Assess the morphology of the erythrocytes.
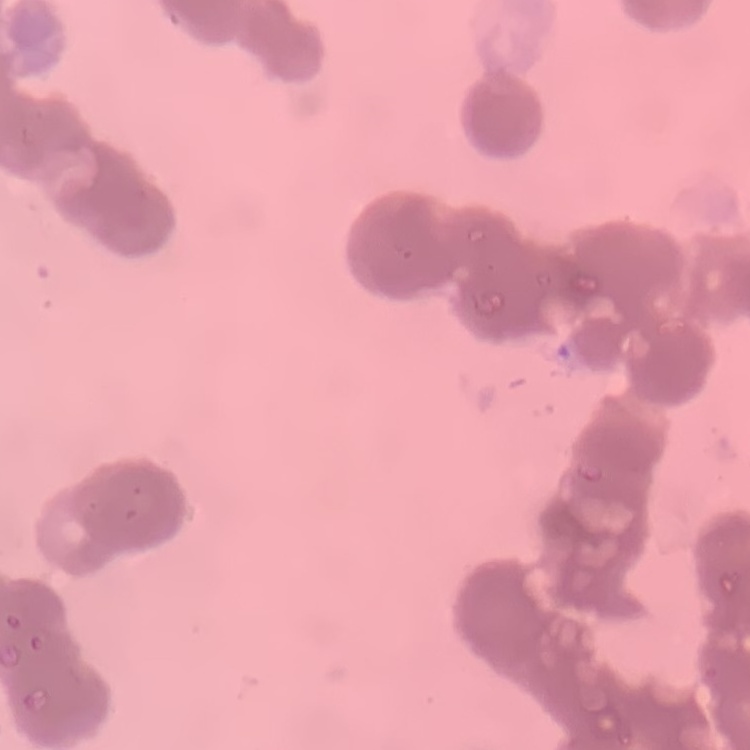
They show rouleaux formation.

Summary:
  - Preparation: thin blood smear
  - Stain: Field's or Giemsa
  - Image type: one tile cut from a larger photomicrograph